Locate every Plasmodium falciparum parasite and give its life-cycle stage, and locate every leukocyte and any debris.
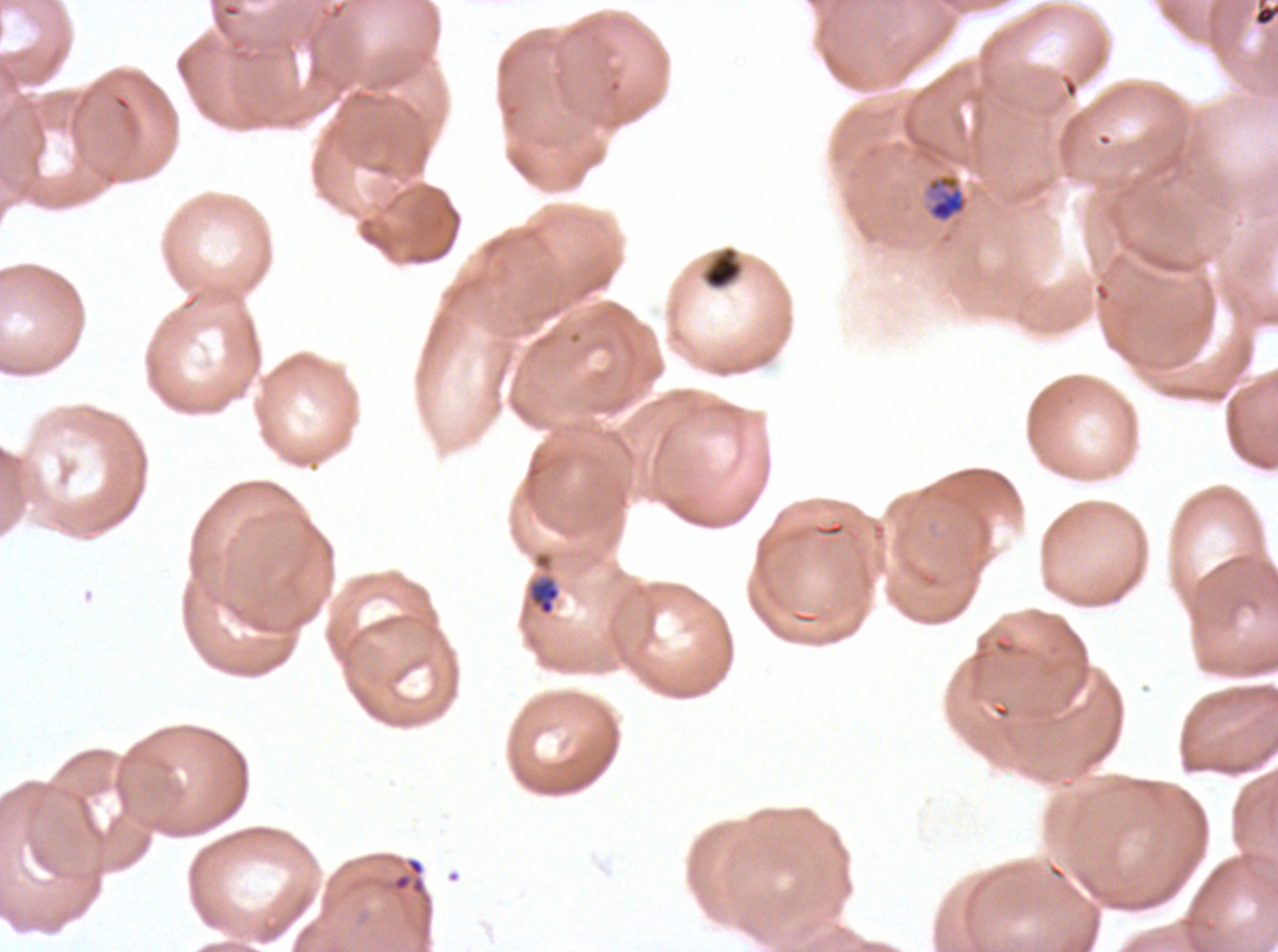
Approximate bounding boxes as (x1, y1, x2, y2) in pixels.
Mid trophozoites: (927, 174, 968, 223).
Early schizonts: (527, 575, 561, 616).
Debris: (1253, 0, 1277, 28), (391, 856, 426, 896).
No rings, late-ring/early-trophozoite forms, late trophozoites, late schizonts, segmenters, gametocytes, or leukocytes observed.

preparation = thin blood smear
life-cycle stages observed = mid trophozoite, early schizont
field of view = sub-image separated from a larger composite
image size = 1278×952 pixels
specimen = Plasmodium falciparum from a patient in The Gambia, cultured ex vivo for 24 to 48 hours
stain = Giemsa